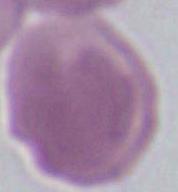 A red blood cell is shown. Captured at 1000x magnification. Micrograph.